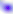
Summary:
  - Identification: Toxoplasma gondii
  - Magnification: 400x
  - Modality: photomicrograph